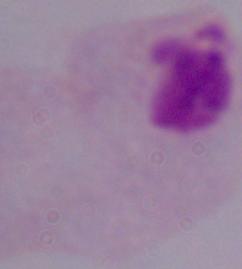

Summary:
  - Modality: micrograph
  - Magnification: 1000x
  - Identification: trichomonad